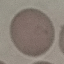
Summary:
  - Result: no malaria parasites detected
  - Image type: cell patch, automatically extracted from a larger field of view and resized to 64 × 64 pixels
  - Stain: Giemsa
  - Capture: smartphone camera at the microscope eyepiece
  - Preparation: thin blood film